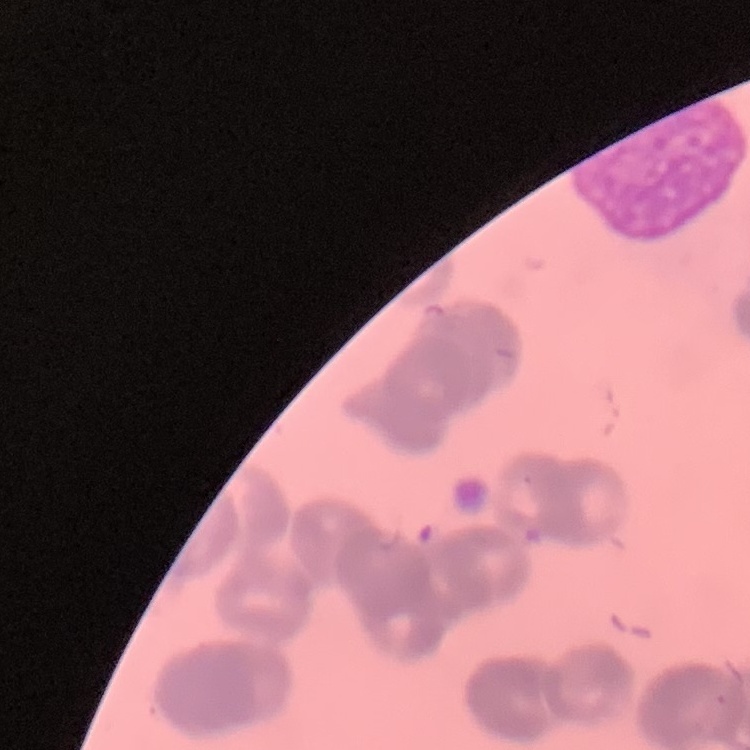

red blood cell morphology = rouleaux formation
preparation = thin blood film
stain = Field's or Giemsa
image type = square crop of a larger photomicrograph